Name the blood parasite species.
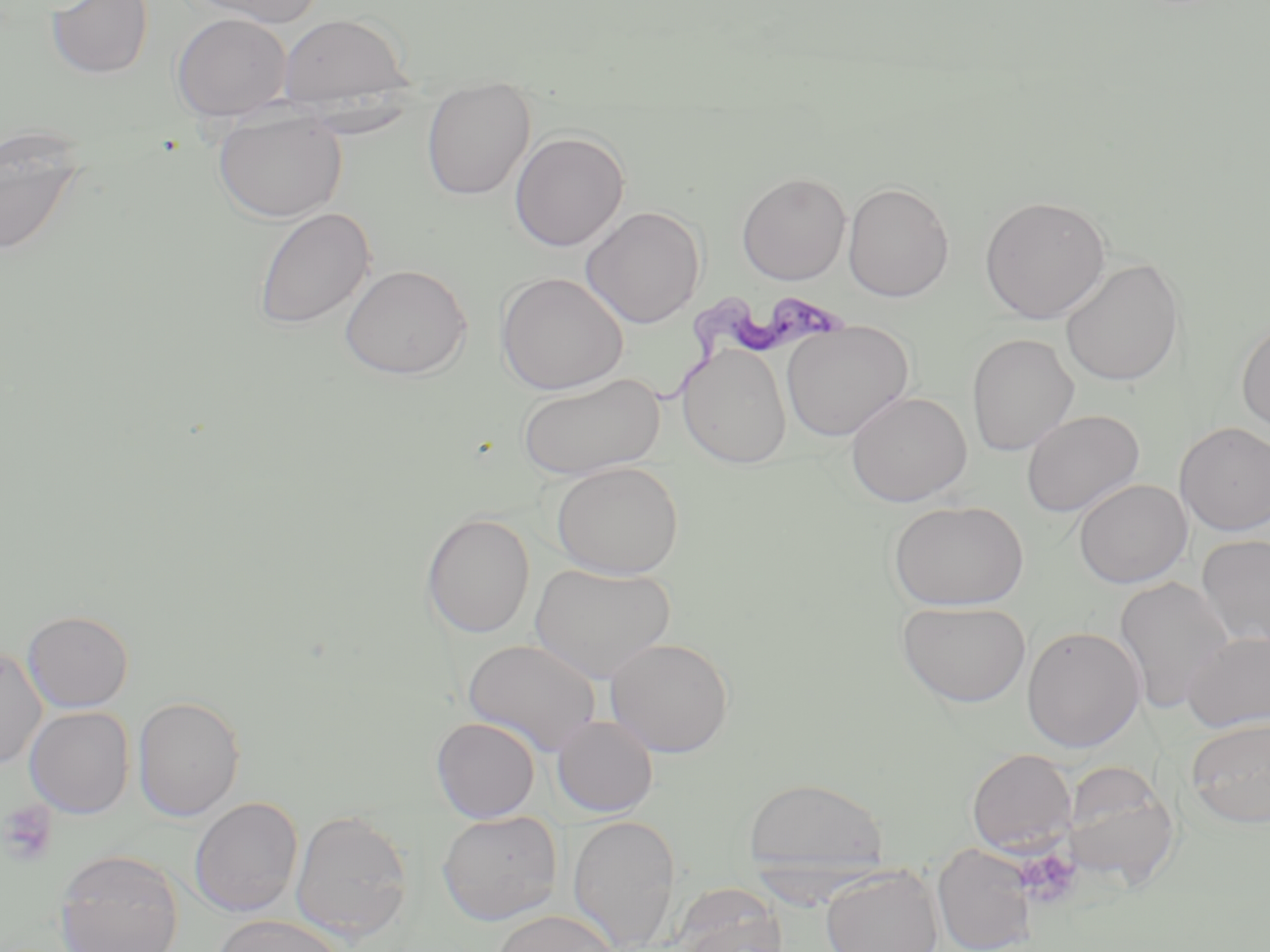
Trypanosoma brucei.

Approximate bounding boxes as named x1/y1/x2/y2 corners in pixels. Trypanosoma brucei locations: (x1=649, y1=289, x2=845, y2=412). Uninfected red blood cell locations: (x1=46, y1=0, x2=154, y2=79), (x1=188, y1=0, x2=325, y2=28), (x1=172, y1=12, x2=291, y2=122), (x1=277, y1=13, x2=413, y2=109), (x1=421, y1=77, x2=536, y2=201), (x1=212, y1=109, x2=347, y2=223), (x1=0, y1=125, x2=89, y2=258), (x1=509, y1=131, x2=630, y2=252), (x1=736, y1=172, x2=851, y2=285), (x1=843, y1=182, x2=955, y2=302), (x1=980, y1=196, x2=1111, y2=324), (x1=581, y1=205, x2=706, y2=329), (x1=254, y1=207, x2=376, y2=330), (x1=1060, y1=257, x2=1184, y2=387), (x1=339, y1=263, x2=472, y2=380), (x1=496, y1=271, x2=629, y2=395), (x1=1236, y1=317, x2=1270, y2=437), (x1=780, y1=321, x2=914, y2=441), (x1=966, y1=333, x2=1080, y2=457), (x1=677, y1=343, x2=792, y2=468), (x1=516, y1=372, x2=665, y2=480), (x1=845, y1=391, x2=972, y2=506), (x1=1021, y1=409, x2=1145, y2=518), (x1=1175, y1=422, x2=1270, y2=536), (x1=550, y1=461, x2=684, y2=579), (x1=1074, y1=479, x2=1192, y2=588), (x1=888, y1=500, x2=1028, y2=611), (x1=421, y1=512, x2=535, y2=638), (x1=1196, y1=534, x2=1270, y2=649), (x1=529, y1=562, x2=675, y2=683), (x1=1114, y1=575, x2=1235, y2=711), (x1=896, y1=600, x2=1032, y2=708), (x1=22, y1=610, x2=134, y2=712), (x1=1021, y1=625, x2=1145, y2=753), (x1=1182, y1=630, x2=1270, y2=733), (x1=605, y1=637, x2=734, y2=757), (x1=462, y1=638, x2=602, y2=756), (x1=0, y1=648, x2=47, y2=769), (x1=132, y1=695, x2=245, y2=821), (x1=25, y1=706, x2=134, y2=818), (x1=552, y1=715, x2=659, y2=817), (x1=431, y1=716, x2=541, y2=823), (x1=1186, y1=717, x2=1270, y2=828), (x1=966, y1=748, x2=1077, y2=855), (x1=1060, y1=761, x2=1180, y2=889), (x1=742, y1=777, x2=889, y2=872), (x1=190, y1=797, x2=302, y2=917), (x1=290, y1=808, x2=413, y2=944), (x1=437, y1=811, x2=562, y2=925), (x1=567, y1=814, x2=681, y2=952), (x1=932, y1=844, x2=1038, y2=952), (x1=54, y1=850, x2=184, y2=952), (x1=821, y1=864, x2=944, y2=952), (x1=667, y1=883, x2=789, y2=952), (x1=491, y1=909, x2=620, y2=952), (x1=211, y1=914, x2=348, y2=952). Platelet locations: (x1=1, y1=799, x2=57, y2=866), (x1=1016, y1=848, x2=1082, y2=908). Single field of view. 1000x magnification. Optical microscopy. May-Grünwald-Giemsa stain. Image is 1270×952 pixels. Thin blood film.